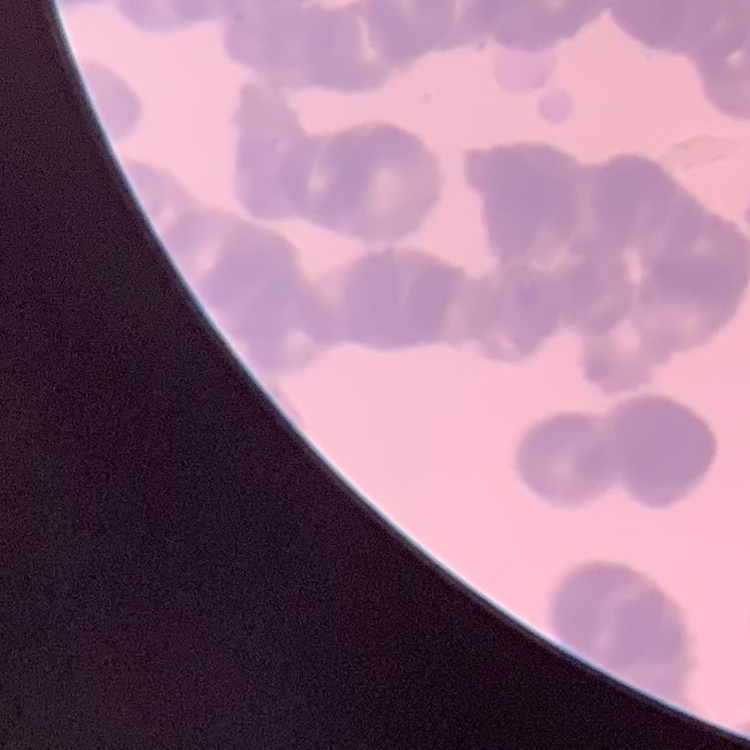

red blood cell morphology = rouleaux formation
image type = one tile cut from a larger photomicrograph
preparation = thin peripheral smear
stain = Field's or Giemsa